Comment on the morphology of the erythrocytes.
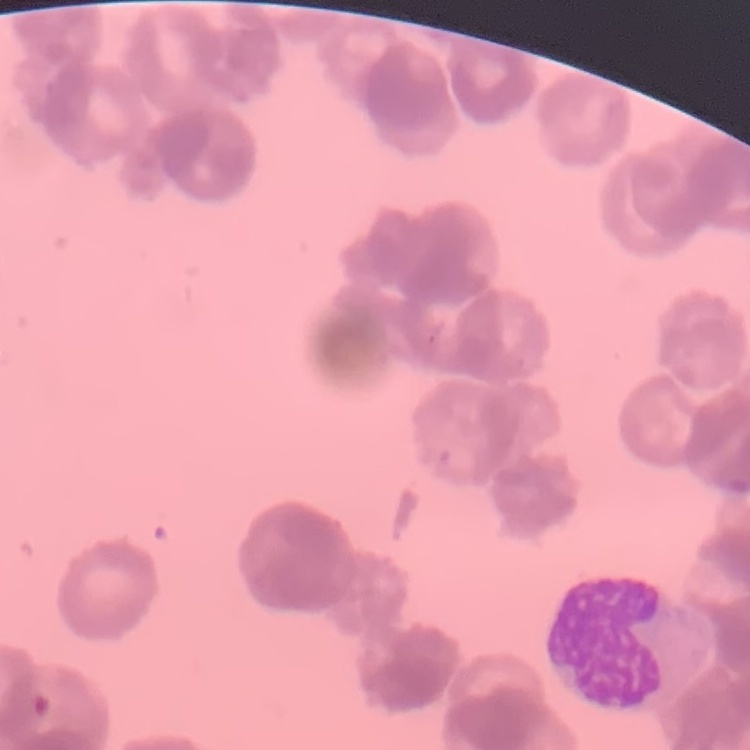
Rouleaux formation.

Stained with either Field's or Giemsa. Thin peripheral smear. One tile cut from a larger photomicrograph.